Assess this cell for malaria.
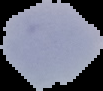

Uninfected.

preparation = thin blood film
image type = cell region segmented out of the field of view; surrounding area masked to black
image size = 103×91 pixels